Locate every Plasmodium falciparum-infected red blood cell.
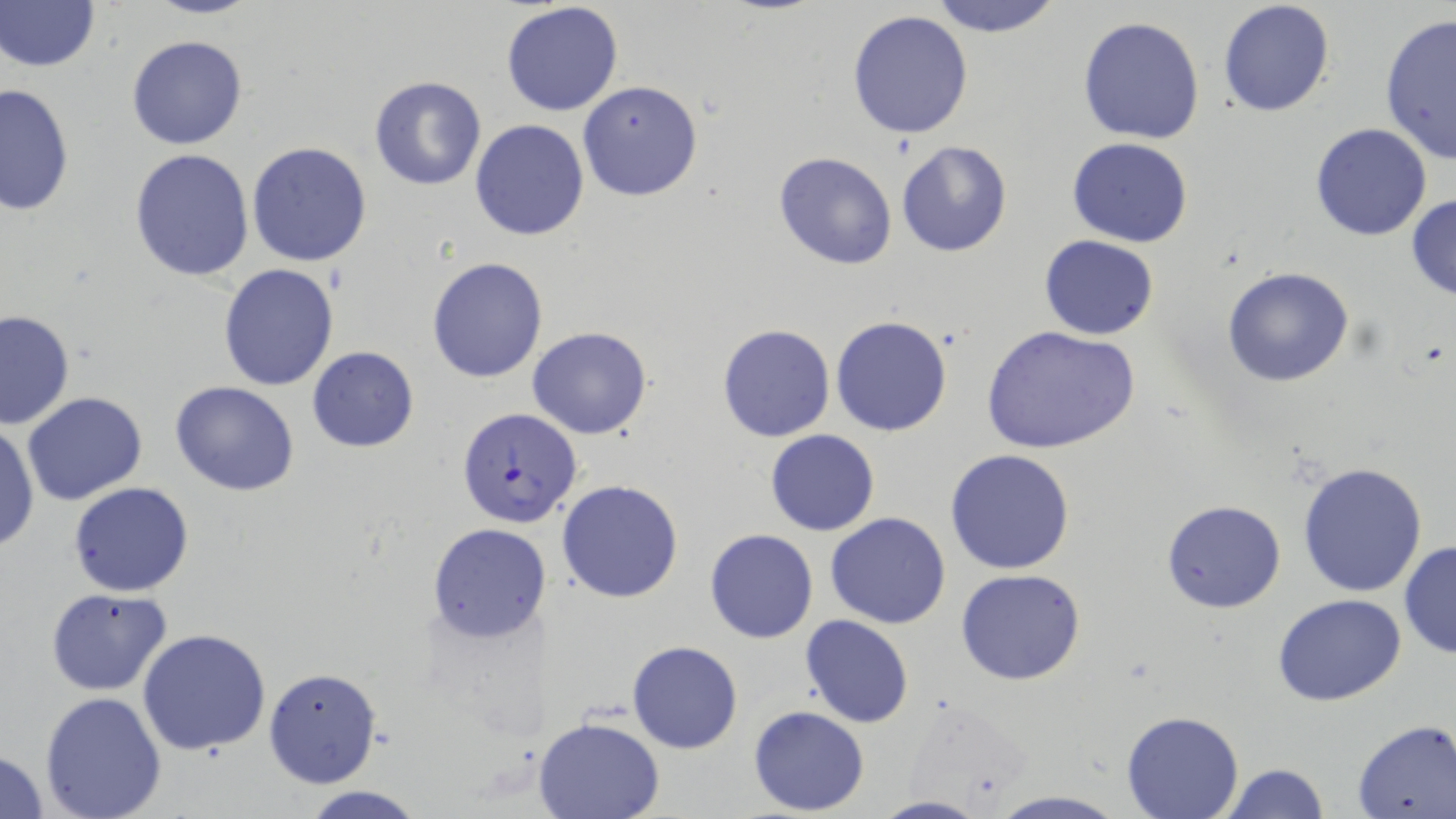
Approximate bounding boxes as [x1, y1, x2, y2] in pixels.
Plasmodium falciparum-infected red blood cells: [457, 407, 581, 528].

slide-level diagnosis = Plasmodium falciparum
stain = May-Grünwald-Giemsa
preparation = thin blood smear
field of view = single
modality = light microscopy
image size = 1456×819 pixels
uninfected red blood cell locations = approximate bounding boxes as [x1, y1, x2, y2] in pixels: [147, 0, 260, 19], [925, 0, 1063, 38], [1217, 0, 1336, 119], [1, 1, 100, 74], [500, 2, 625, 117], [846, 9, 974, 140], [1379, 12, 1456, 165], [1077, 16, 1206, 144], [126, 34, 248, 151], [368, 75, 487, 191], [577, 81, 704, 202], [1, 84, 75, 215], [470, 118, 591, 241], [1309, 121, 1433, 240], [1066, 136, 1193, 248], [895, 139, 1014, 258], [247, 141, 374, 267], [129, 149, 255, 281], [772, 151, 897, 271], [1406, 193, 1456, 302], [1040, 236, 1159, 340], [426, 256, 549, 382], [217, 262, 340, 391], [1222, 267, 1353, 387], [0, 310, 74, 430], [831, 315, 952, 436], [717, 323, 836, 441], [980, 325, 1141, 454], [527, 326, 653, 440], [307, 346, 419, 451], [171, 382, 300, 496], [22, 392, 147, 507], [0, 423, 40, 555], [764, 429, 880, 536], [945, 448, 1075, 574], [1297, 460, 1428, 597], [557, 480, 685, 603], [67, 481, 194, 597], [1161, 500, 1287, 613], [825, 513, 951, 628], [428, 523, 552, 644], [703, 528, 817, 644], [1399, 540, 1456, 660], [954, 568, 1085, 687], [45, 587, 172, 695], [1273, 594, 1407, 707], [799, 616, 915, 728], [139, 628, 271, 755], [628, 640, 742, 754], [263, 666, 382, 789], [38, 691, 167, 819], [748, 706, 871, 815], [1121, 712, 1245, 819], [534, 717, 665, 819], [1351, 719, 1455, 818], [0, 748, 51, 817], [1220, 762, 1329, 818], [295, 784, 429, 819], [988, 790, 1129, 819], [871, 795, 988, 818]
magnification = 1000x